Assess this cell for malaria.
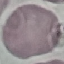

Uninfected.

{
  "preparation": "thin blood film",
  "capture": "smartphone through the microscope eyepiece",
  "image_type": "cell patch, automatically extracted from a larger field of view and resized to 64 × 64 pixels",
  "stain": "Giemsa"
}